Name the parasite shown.
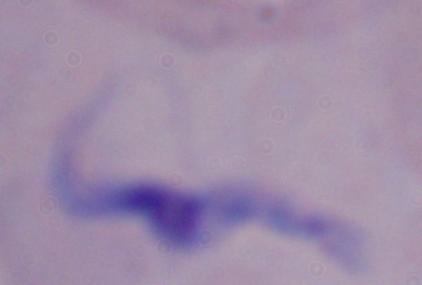
This is a trypanosome.

Summary:
  - Modality: micrograph
  - Magnification: 1000x